Identify the preparation type.
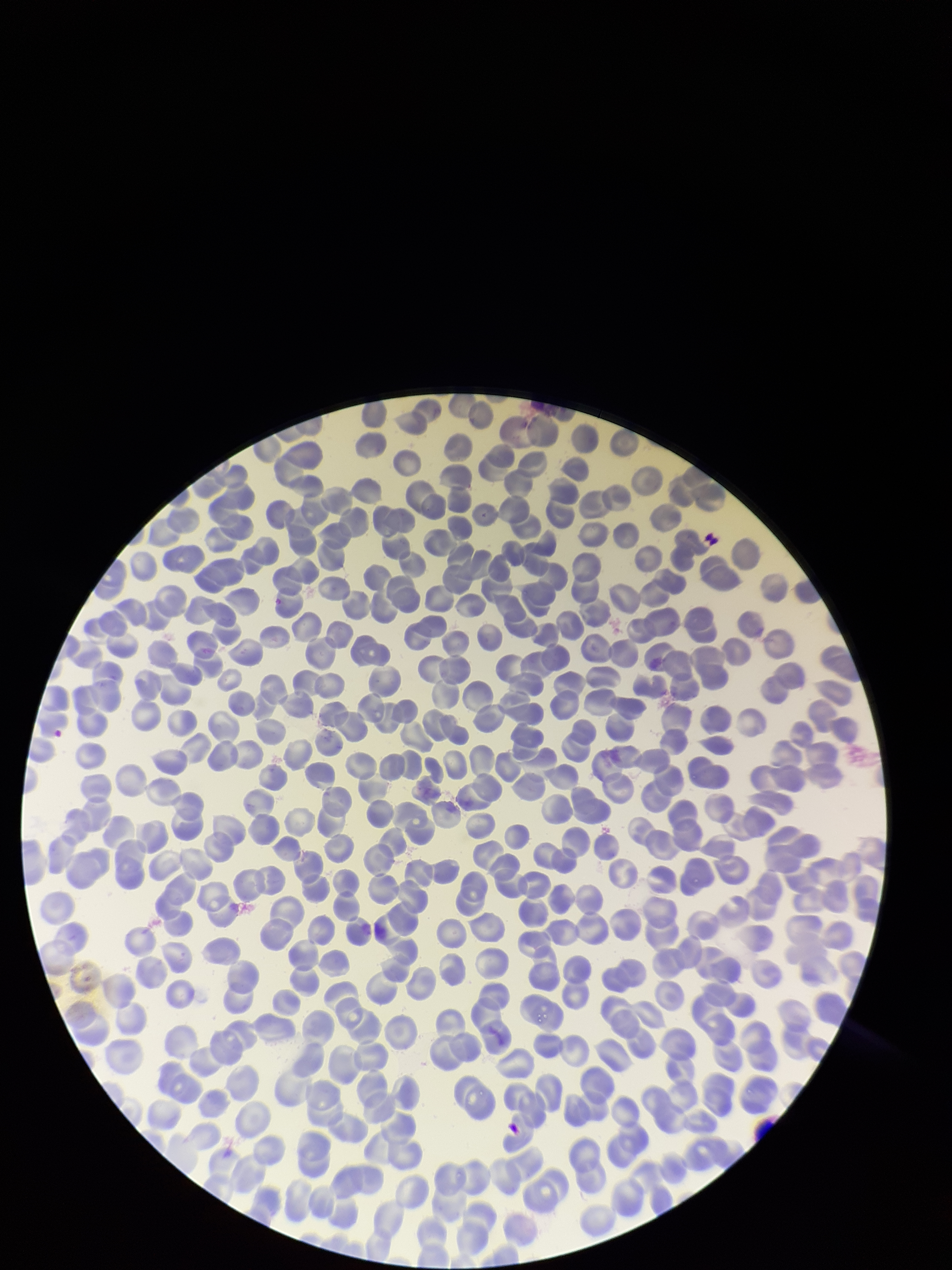
A thin smear.

parasitized red blood cell count = 0
field of view = one from this slide
stain = Giemsa
patient malaria status = negative
red blood cell count = 337
image size = 952×1270 pixels
parasitized red blood cells = none identified
capture = smartphone photograph through the microscope eyepiece